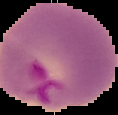
image type = segmented cell region on a black background
malaria status = parasitized
preparation = thin blood film
image size = 118×115 pixels